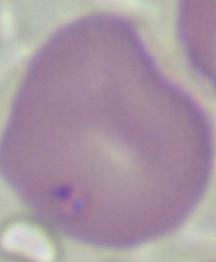
identification = Babesia
modality = micrograph
magnification = 1000x